Assess this cell for malaria.
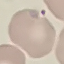
Parasitized.

Giemsa stain. Thin blood film. Automatically extracted cell patch, resized to 64 × 64 pixels. Acquired by smartphone through the microscope eyepiece.